Assess this cell for malaria.
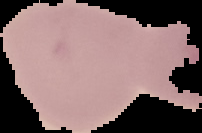

Uninfected.

Summary:
  - Preparation: thin blood smear
  - Image type: segmented cell region with the area outside set to black
  - Image size: 202×133 pixels